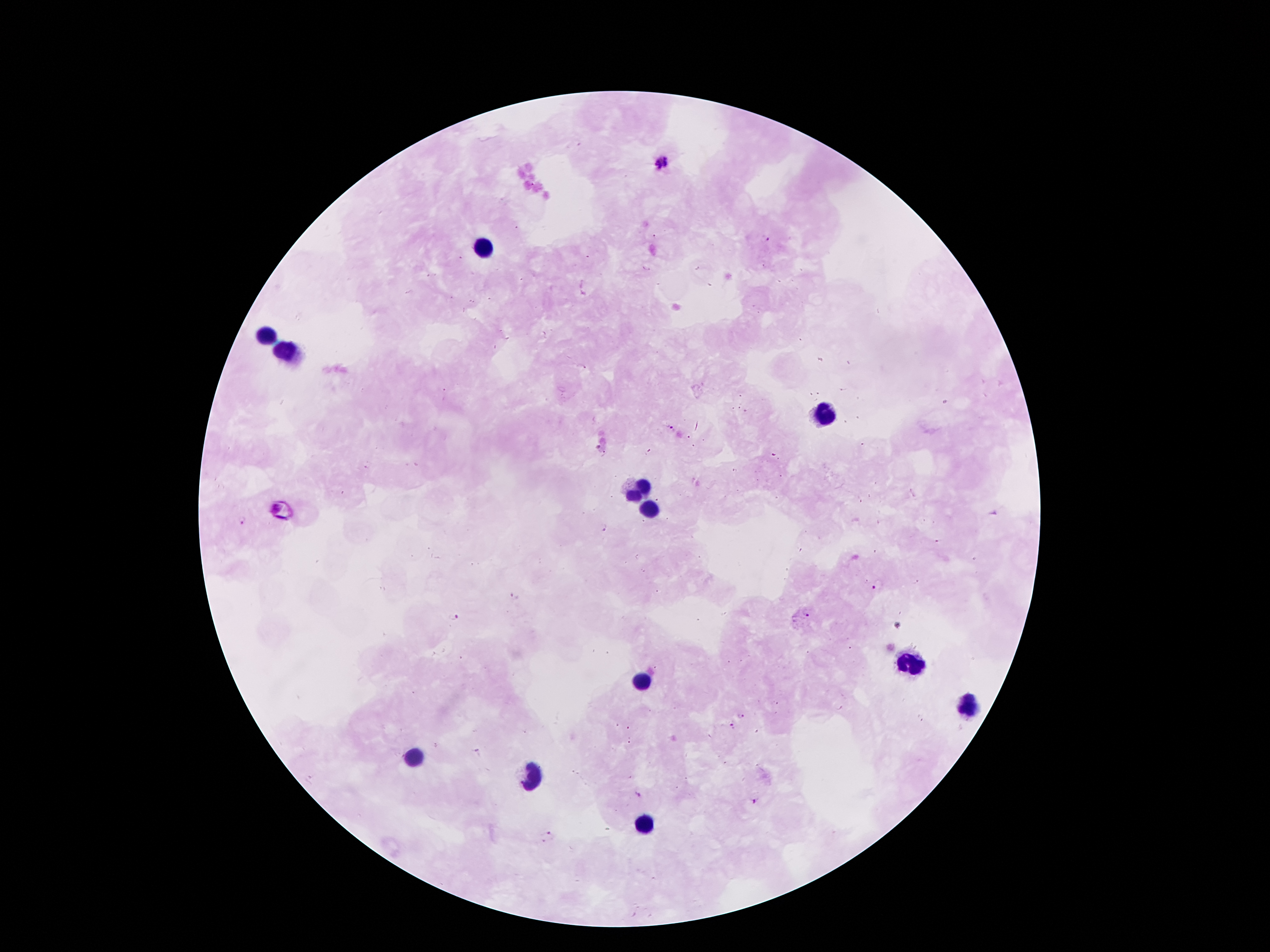
Approximate object centers, in pixels from the top-left corner.
Summary:
  - Plasmodium parasite locations: (x=665, y=162), (x=766, y=240), (x=582, y=367), (x=671, y=428), (x=598, y=447), (x=649, y=453), (x=772, y=453), (x=603, y=455), (x=275, y=508), (x=245, y=522), (x=603, y=527), (x=879, y=585), (x=514, y=596), (x=806, y=615), (x=453, y=617), (x=741, y=716), (x=733, y=726), (x=638, y=795), (x=755, y=801), (x=547, y=836)
  - Leukocyte locations: (x=483, y=245), (x=267, y=337), (x=289, y=353), (x=824, y=411), (x=639, y=485), (x=655, y=509), (x=907, y=661), (x=641, y=679), (x=972, y=707), (x=415, y=757), (x=529, y=777), (x=647, y=821)
  - Stain: Giemsa
  - Patient malaria status: infected with Plasmodium falciparum
  - Capture: smartphone through the microscope eyepiece
  - Preparation: thick blood film
  - Field of view: one from this slide
  - Magnification: 100x
  - Image size: 1270×952 pixels